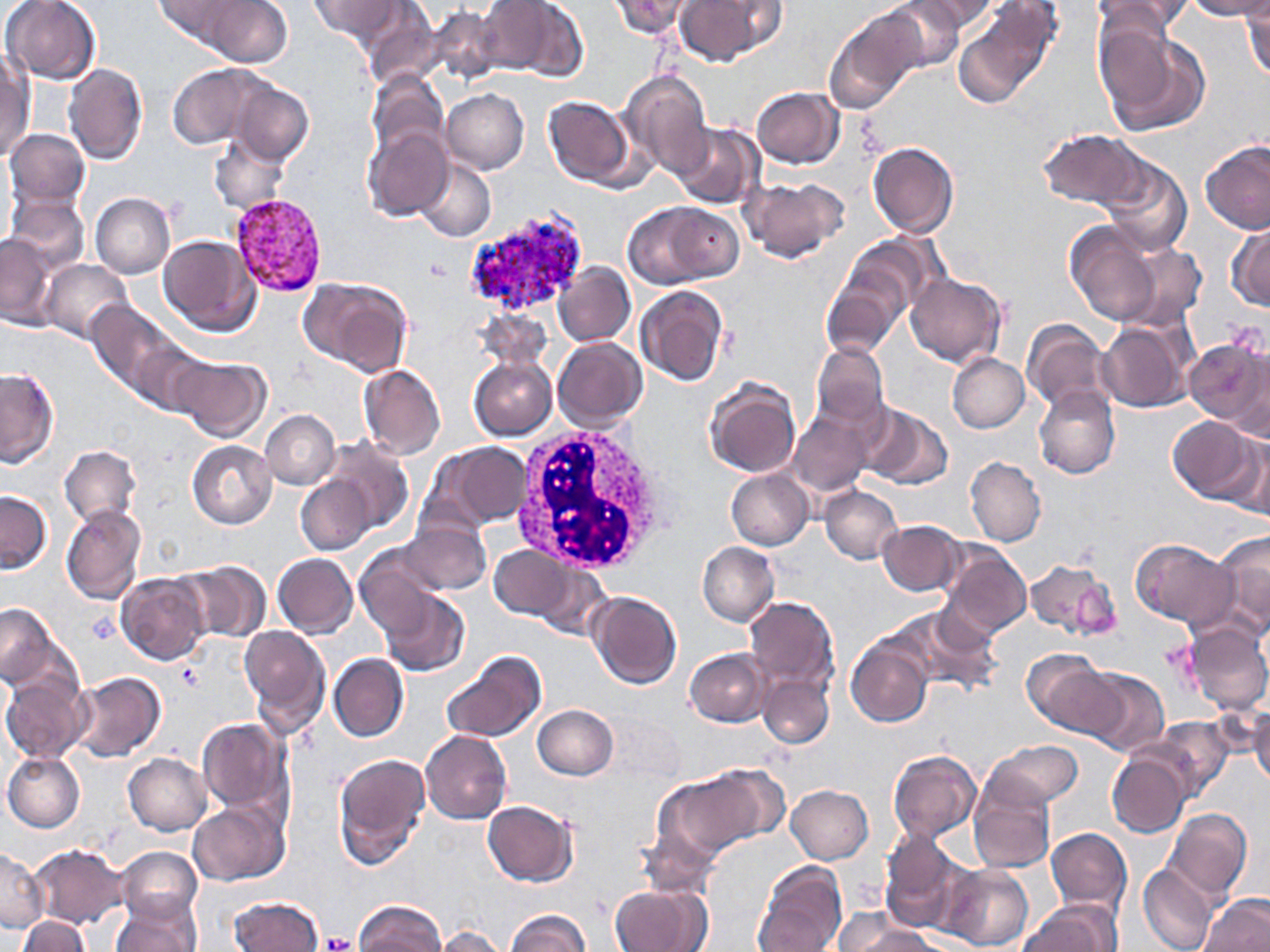

Summary:
  - Coordinate format: approximate bounding boxes as [x1, y1, x2, y2] in pixels
  - Plasmodium vivax-infected red blood cell locations: [229, 193, 330, 299], [463, 209, 590, 317]
  - White blood cell locations: [509, 422, 675, 576]
  - Platelet locations: [423, 257, 453, 284], [86, 613, 121, 645], [177, 664, 204, 689], [322, 933, 355, 952]
  - Uninfected red blood cell locations: [153, 0, 248, 50], [201, 0, 292, 68], [309, 0, 400, 42], [479, 0, 583, 78], [609, 0, 694, 40], [674, 0, 784, 65], [880, 0, 966, 72], [910, 0, 1000, 34], [1090, 0, 1194, 43], [1184, 0, 1270, 20], [1, 1, 102, 84], [1242, 1, 1270, 81], [356, 2, 440, 88], [428, 6, 504, 87], [956, 7, 1056, 109], [826, 9, 924, 113], [1096, 23, 1208, 136], [0, 52, 33, 160], [63, 64, 147, 165], [167, 64, 266, 150], [618, 69, 714, 176], [366, 70, 449, 161], [227, 78, 314, 166], [752, 87, 844, 168], [442, 89, 529, 174], [543, 96, 635, 188], [670, 123, 762, 209], [362, 124, 453, 220], [4, 128, 90, 210], [1037, 128, 1146, 210], [209, 134, 290, 215], [1201, 139, 1270, 234], [868, 142, 959, 238], [1096, 155, 1192, 255], [413, 158, 496, 242], [742, 176, 850, 264], [90, 192, 175, 278], [6, 195, 89, 272], [623, 200, 739, 287], [1064, 218, 1173, 327], [1228, 222, 1270, 310], [0, 234, 57, 328], [841, 234, 939, 324], [158, 235, 259, 336], [41, 259, 132, 343], [555, 263, 635, 347], [822, 268, 908, 358], [905, 271, 1006, 368], [299, 277, 412, 377], [635, 285, 728, 386], [86, 302, 172, 391], [1096, 319, 1194, 413], [1022, 320, 1112, 414], [1185, 336, 1268, 433], [552, 338, 647, 431], [126, 340, 212, 418], [810, 344, 889, 430], [947, 353, 1029, 433], [171, 355, 272, 442], [468, 356, 556, 440], [358, 364, 445, 459], [0, 369, 59, 467], [705, 377, 801, 478], [1033, 385, 1119, 479], [857, 404, 952, 488], [260, 410, 340, 489], [789, 414, 872, 496], [1168, 417, 1258, 501], [1223, 432, 1270, 516], [320, 438, 412, 531], [187, 440, 276, 528], [432, 442, 530, 530], [60, 446, 141, 527], [965, 457, 1046, 547], [726, 468, 814, 551], [296, 475, 376, 554], [820, 486, 902, 564], [0, 490, 51, 573], [60, 504, 147, 604], [402, 518, 490, 595], [878, 520, 967, 596], [1213, 529, 1270, 633], [1130, 538, 1236, 627], [698, 541, 779, 626], [938, 541, 1032, 639], [489, 545, 575, 620], [355, 547, 443, 635], [272, 553, 357, 638], [176, 560, 272, 642], [1023, 560, 1120, 641], [532, 562, 613, 640], [116, 572, 210, 665], [380, 590, 470, 676], [588, 591, 681, 690], [744, 596, 839, 695], [0, 603, 58, 685], [894, 604, 1001, 694], [1183, 620, 1270, 715], [239, 625, 331, 731], [846, 637, 933, 727], [685, 649, 772, 726], [1024, 651, 1120, 736], [441, 652, 546, 743], [329, 653, 408, 742], [1077, 667, 1169, 756], [70, 671, 165, 763], [0, 674, 90, 763], [758, 674, 833, 749], [1248, 701, 1270, 789], [533, 704, 617, 780], [599, 713, 686, 786], [197, 717, 292, 819], [1146, 717, 1235, 798], [421, 730, 511, 824], [986, 740, 1083, 810], [888, 750, 980, 842], [1107, 751, 1190, 838], [3, 752, 85, 832], [123, 753, 212, 834], [334, 753, 430, 866], [656, 772, 766, 862], [967, 774, 1055, 874], [786, 785, 873, 863], [188, 800, 289, 886], [483, 801, 578, 887], [1164, 809, 1253, 902], [638, 826, 721, 897], [1045, 827, 1131, 914], [880, 830, 969, 932], [28, 844, 129, 928], [117, 847, 202, 924], [0, 850, 48, 932], [754, 861, 847, 952], [1138, 862, 1219, 952], [939, 864, 1033, 951], [610, 885, 709, 952], [1199, 894, 1269, 952], [229, 896, 324, 952], [111, 897, 199, 952], [354, 900, 446, 952], [1020, 900, 1124, 950], [505, 910, 589, 952], [835, 912, 930, 952], [18, 915, 90, 951], [435, 927, 505, 952]
  - Slide-level diagnosis: Plasmodium vivax
  - Image size: 1270×952 pixels
  - Field of view: single
  - Modality: optical microscopy
  - Magnification: 1000x
  - Stain: May-Grünwald-Giemsa
  - Preparation: thin blood smear